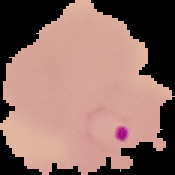
From a thin blood film. Cell region segmented out of the field of view; the surrounding area is masked to black. Malaria status: parasitized. Image is 175×175 pixels.